Comment on the morphology of the erythrocytes.
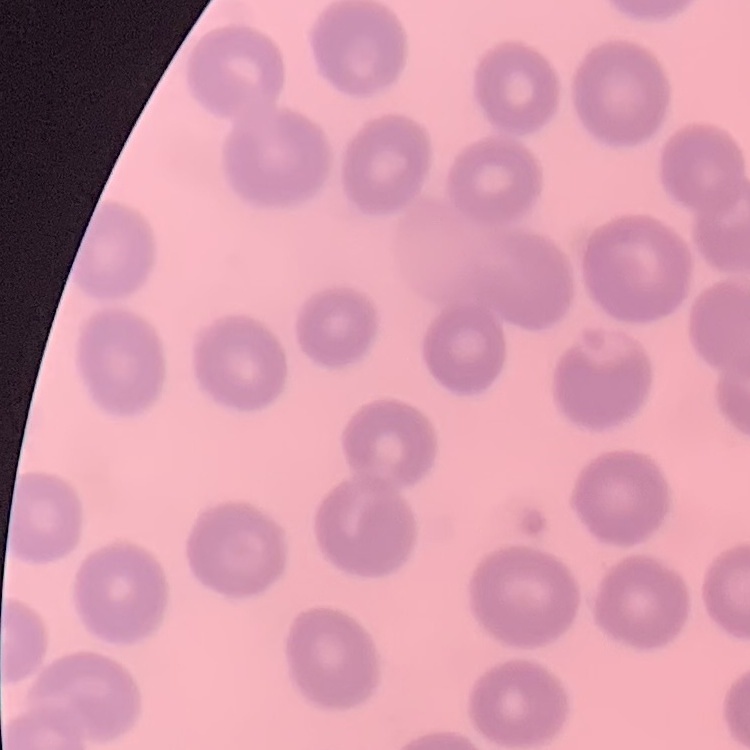

They show no rouleaux formation.

One tile cut from a larger photomicrograph. Thin blood film. Stained with either Field's or Giemsa.